State which cell type is depicted.
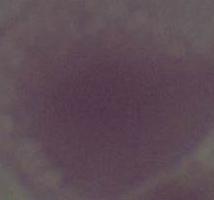

This is an erythrocyte.

magnification = 1000x
modality = micrograph